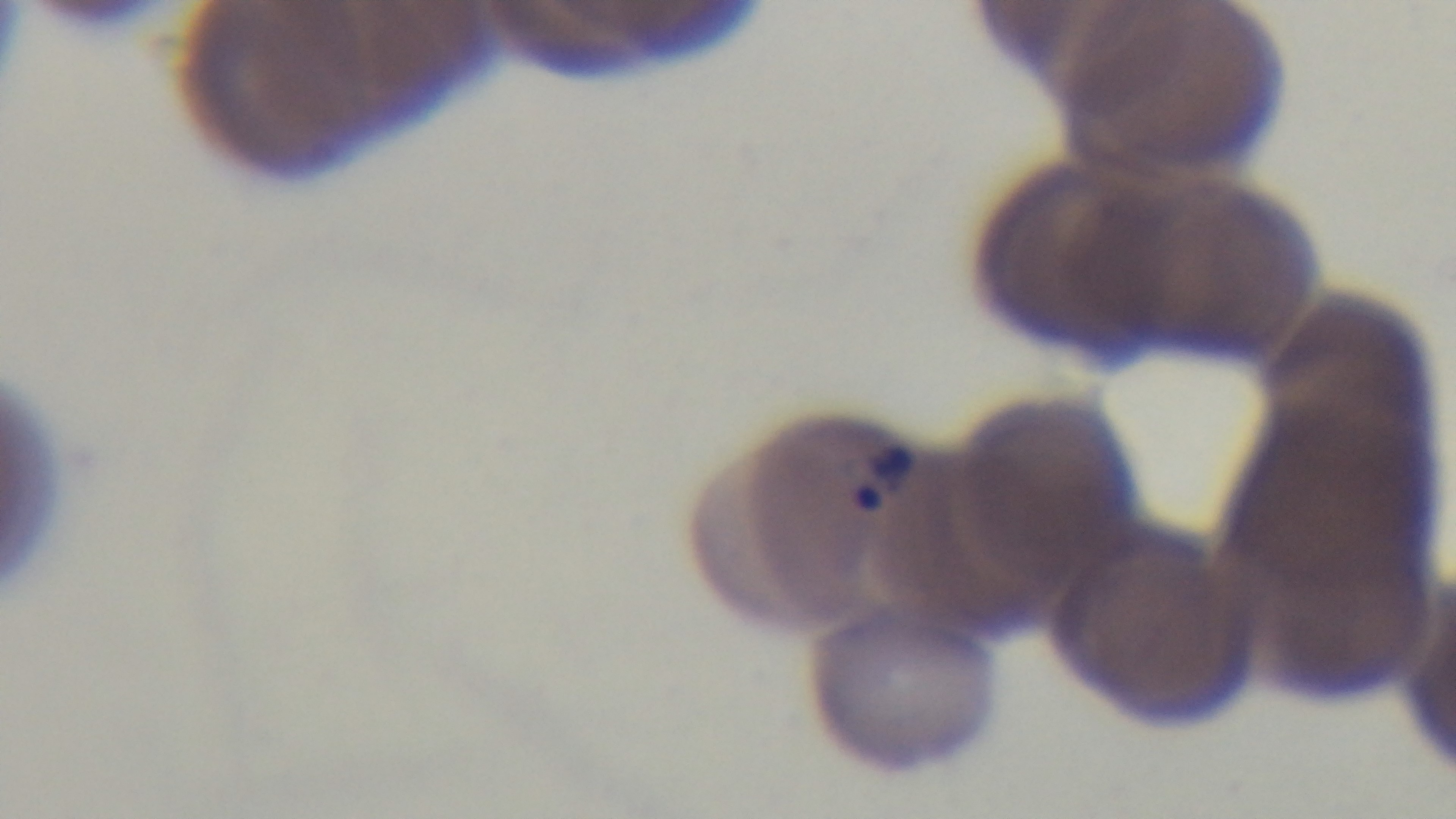
Summary:
  - Malaria status: infected
  - Objective: 100x oil immersion
  - Preparation: thin
  - Field of view: one from the slide
  - Modality: light microscopy
  - Capture: mounted 4K digital camera
  - Stain: Giemsa